Locate every Plasmodium parasite.
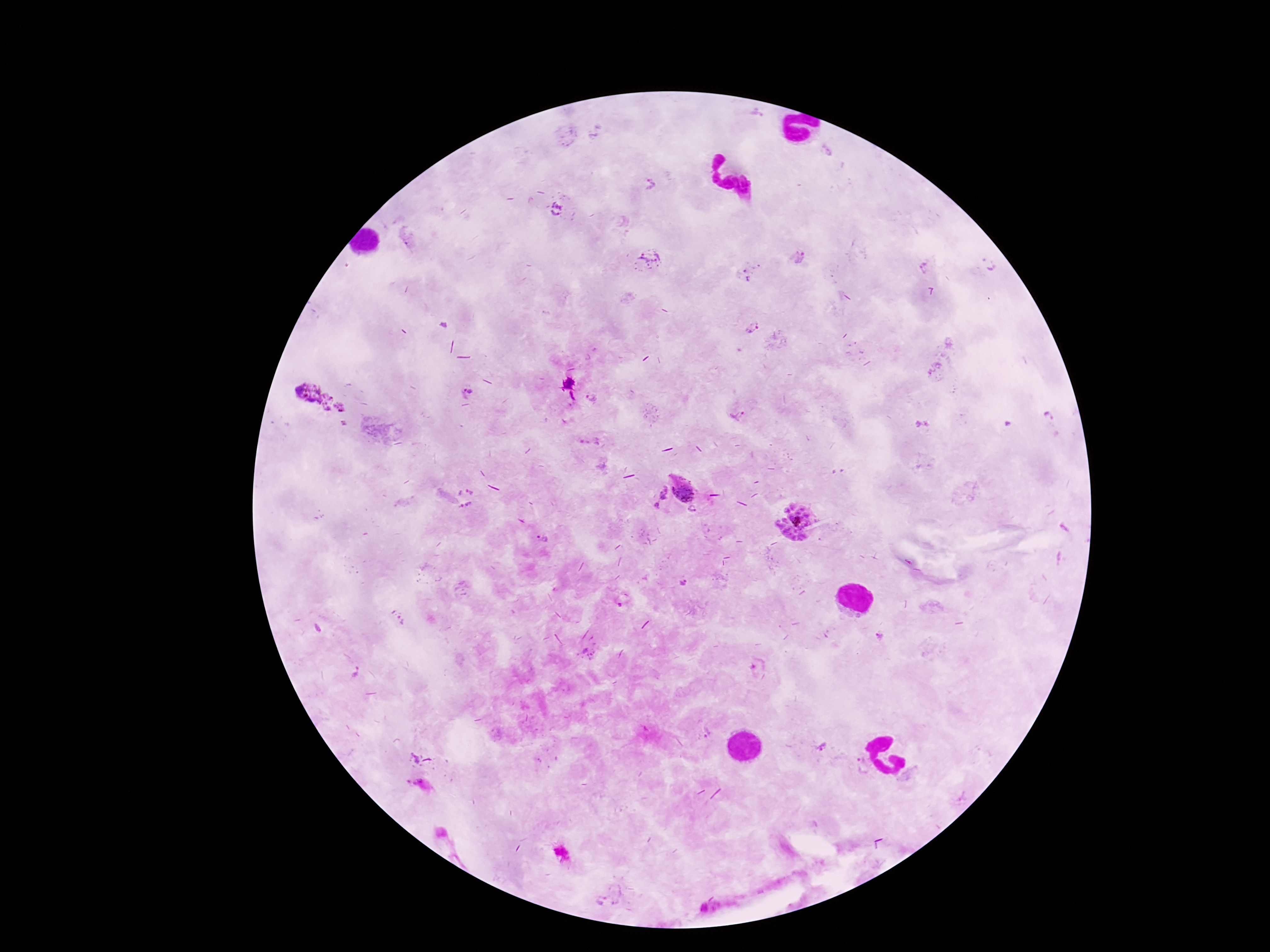

Approximate centers as {x, y} in pixels.
Plasmodium parasites: {650, 184}, {557, 211}, {799, 258}, {649, 261}, {985, 265}, {924, 268}, {745, 270}, {748, 279}, {751, 329}, {467, 391}, {320, 400}, {592, 400}, {738, 416}, {1048, 417}, {683, 489}, {664, 494}, {470, 497}, {657, 505}, {693, 510}, {798, 521}, {541, 538}, {620, 605}, {398, 620}, {357, 671}, {415, 758}, {862, 767}.

Summary:
  - Field of view: one from this slide
  - Capture: smartphone camera through the microscope eyepiece
  - Stain: Giemsa
  - Preparation: thick blood film
  - Patient malaria status: positive
  - Magnification: 100x
  - Image size: 1270×952 pixels